Identify the parasite.
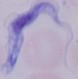

This is a trypanosome.

modality = photomicrograph
magnification = 1000x